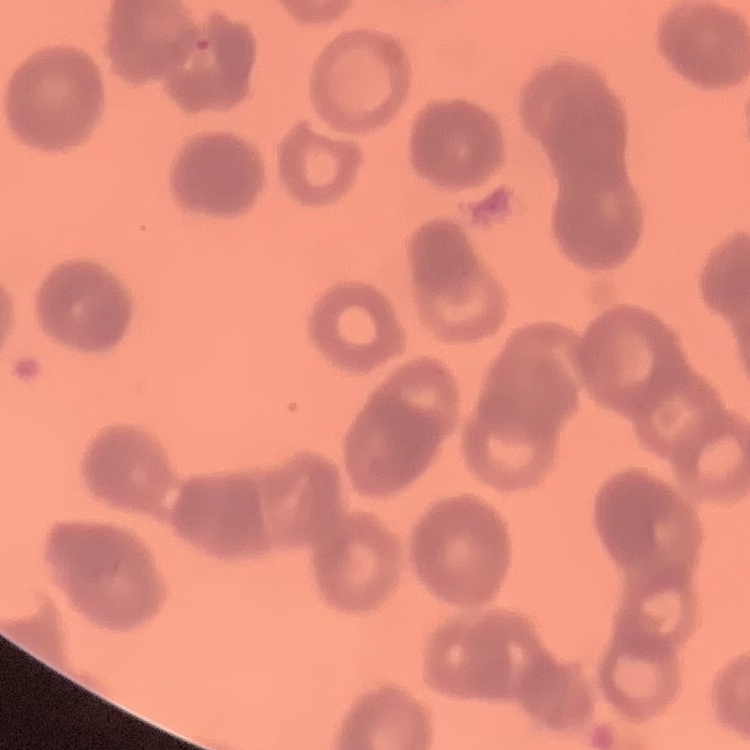 The erythrocytes exhibit rouleaux formation. Stained with either Field's or Giemsa. Thin blood smear. Square crop of a larger photomicrograph.